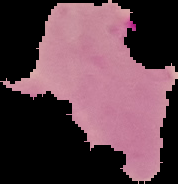
{
  "image_type": "segmented cell region with the area outside set to black",
  "result": "malaria parasites identified",
  "preparation": "thin blood film",
  "image_size": "178×184 pixels"
}